State which cell type is depicted.
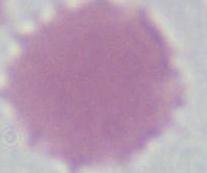
This is an erythrocyte.

Micrograph. Captured at 1000x magnification.